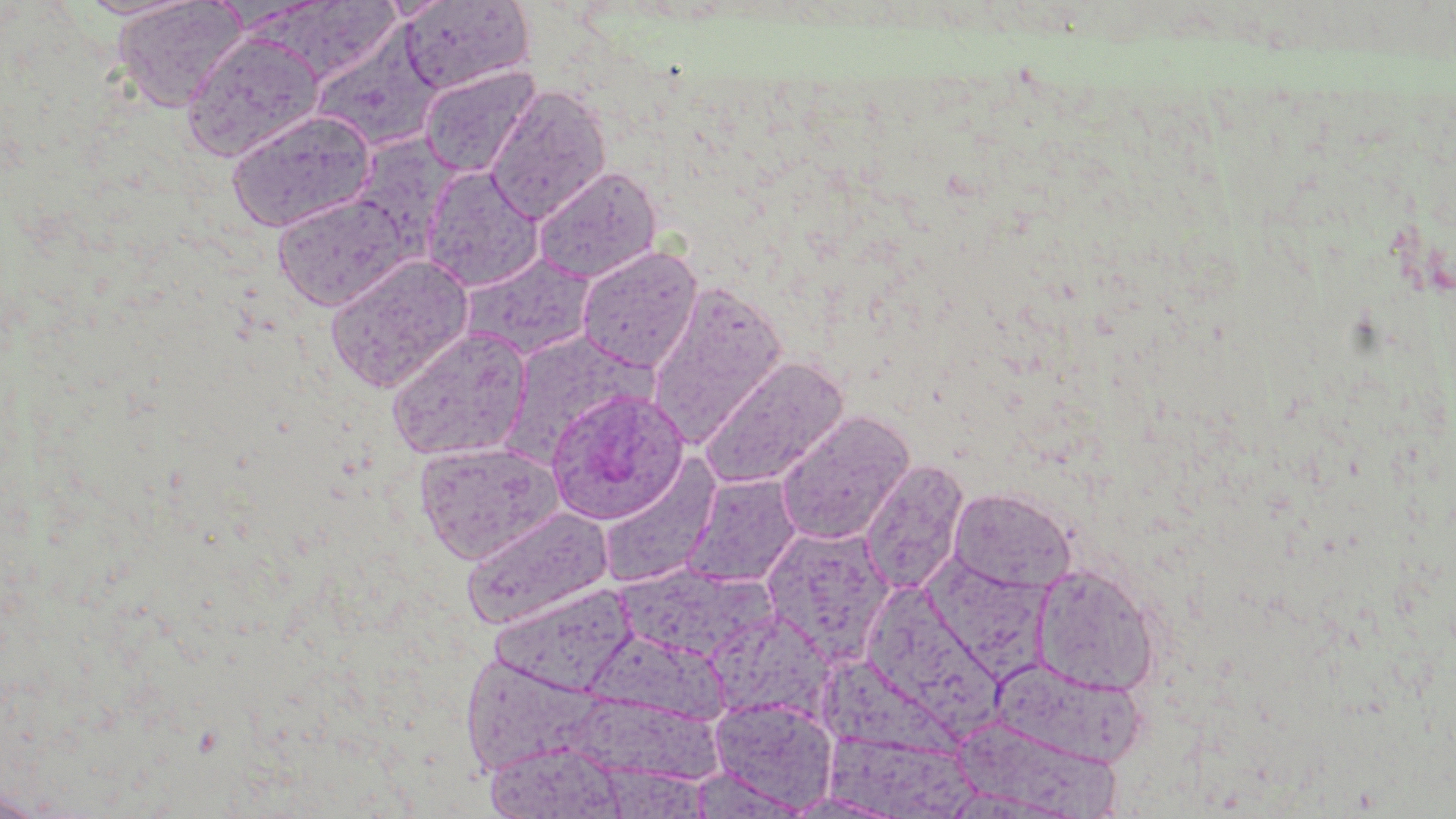
slide-level diagnosis = Plasmodium ovale
image size = 1456×819 pixels
preparation = thin blood film
modality = optical microscopy
stain = May-Grünwald-Giemsa
Plasmodium ovale-infected red blood cell locations = approximate bounding boxes as [x1, y1, x2, y2] in pixels: [545, 388, 690, 524]
magnification = 1000x
uninfected red blood cell locations = approximate bounding boxes as [x1, y1, x2, y2] in pixels: [74, 0, 203, 20], [112, 0, 247, 112], [400, 1, 533, 95], [313, 23, 446, 153], [181, 31, 325, 162], [419, 64, 541, 178], [486, 86, 611, 225], [225, 109, 377, 233], [353, 131, 469, 251], [422, 166, 544, 292], [532, 166, 662, 283], [271, 191, 414, 311], [576, 246, 702, 373], [460, 253, 596, 361], [324, 254, 474, 394], [646, 281, 788, 448], [385, 326, 533, 463], [500, 330, 652, 468], [699, 357, 849, 490], [775, 411, 915, 545], [413, 441, 562, 564], [598, 457, 722, 590], [860, 459, 970, 597], [682, 473, 802, 588], [948, 487, 1078, 593], [460, 506, 613, 630], [761, 525, 894, 661], [924, 550, 1055, 687], [617, 564, 771, 663], [1031, 564, 1161, 696], [493, 582, 642, 699], [867, 584, 1007, 738], [709, 619, 851, 726], [589, 625, 739, 725], [814, 653, 983, 782], [462, 655, 603, 781], [991, 659, 1147, 766], [709, 697, 838, 812], [568, 699, 732, 784], [957, 722, 1122, 817], [821, 731, 982, 817], [485, 740, 626, 818], [0, 786, 48, 819]
field of view = one of a larger specimen